State which parasite is depicted.
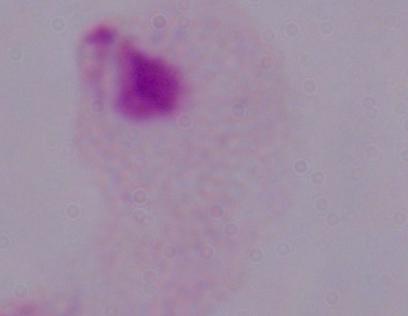
This is a trichomonad.

Photomicrograph. Captured at 1000x magnification.